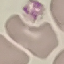

{
  "result": "no malaria parasites detected",
  "preparation": "thin blood smear",
  "stain": "Giemsa",
  "image_type": "cell patch, automatically extracted from a larger field of view and resized to 64 × 64 pixels",
  "capture": "smartphone through the microscope eyepiece"
}